Assess this cell for malaria.
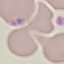
It is parasitized.

Cell patch, automatically extracted from a larger field of view and resized to 64 × 64 pixels. Giemsa-stained preparation. Photographed with a smartphone camera at the microscope eyepiece. Thin blood film.